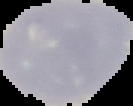

Summary:
  - Preparation: thin blood smear
  - Result: negative for malaria parasites
  - Image type: segmented cell region with the area outside set to black
  - Image size: 133×106 pixels